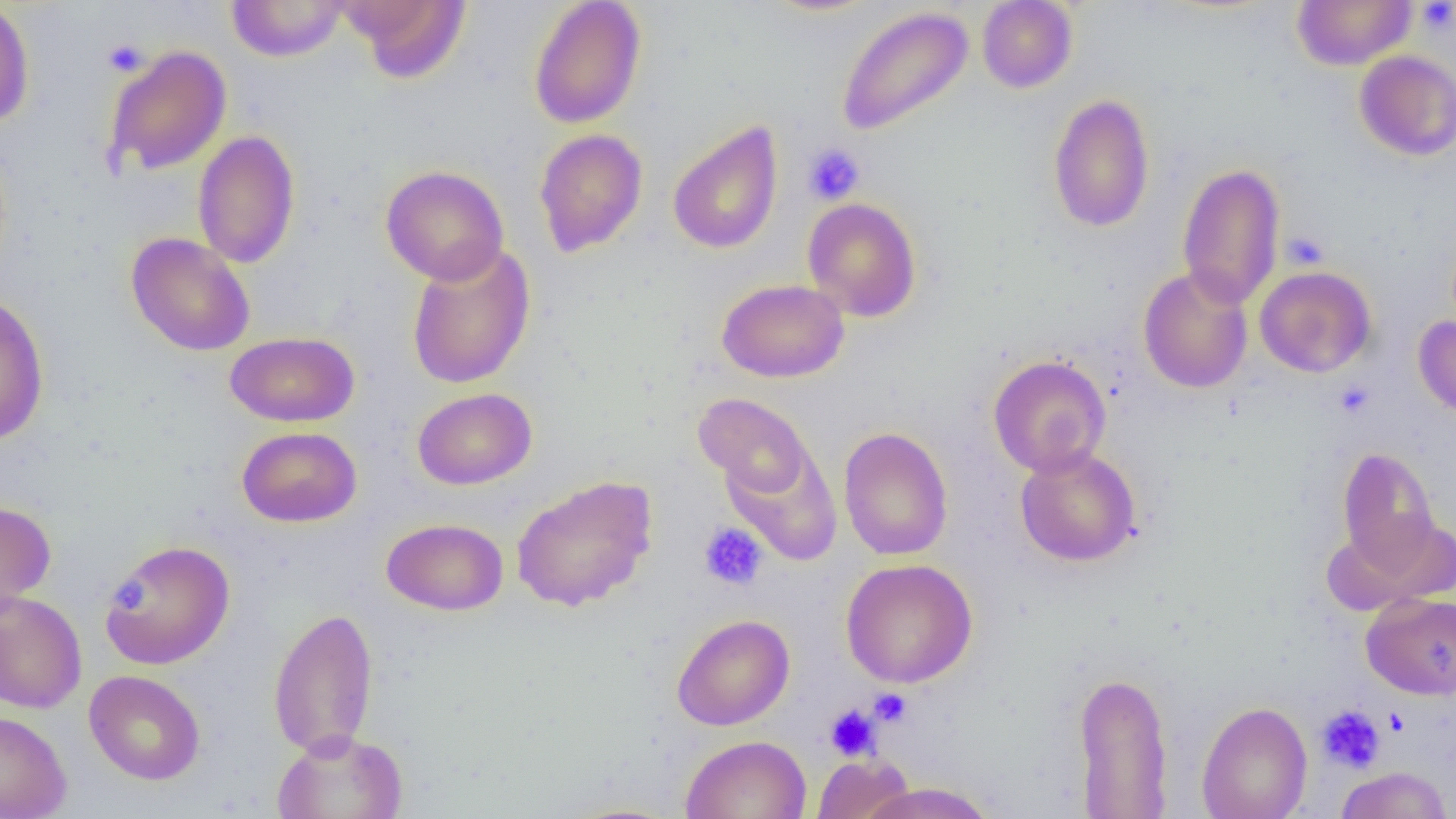

Summary:
  - Coordinate format: approximate bounding boxes as [x1, y1, x2, y2] in pixels
  - Platelet locations: [1416, 1, 1456, 34], [103, 39, 148, 76], [802, 143, 866, 204], [1281, 231, 1329, 270], [1334, 381, 1374, 419], [699, 522, 768, 591], [108, 579, 146, 614], [869, 688, 911, 726], [824, 704, 881, 761], [1316, 704, 1386, 774], [1384, 708, 1410, 737]
  - Uninfected red blood cell locations: [0, 0, 35, 128], [338, 0, 472, 83], [529, 0, 647, 129], [760, 0, 883, 17], [977, 0, 1078, 92], [1291, 0, 1416, 70], [226, 1, 349, 62], [836, 5, 974, 137], [104, 45, 232, 176], [1354, 50, 1456, 160], [1047, 94, 1155, 233], [667, 121, 783, 255], [534, 128, 648, 258], [192, 130, 301, 269], [1176, 163, 1286, 308], [380, 165, 510, 286], [803, 197, 922, 322], [126, 232, 255, 356], [406, 240, 536, 390], [1138, 266, 1253, 393], [1254, 266, 1376, 377], [717, 278, 849, 383], [0, 292, 49, 445], [1413, 316, 1456, 418], [224, 331, 359, 427], [988, 355, 1111, 477], [412, 387, 537, 490], [693, 392, 815, 500], [237, 426, 362, 527], [838, 426, 953, 561], [721, 445, 842, 566], [1015, 446, 1142, 567], [1337, 448, 1440, 572], [511, 475, 658, 612], [0, 500, 56, 616], [1329, 515, 1454, 614], [381, 517, 508, 615], [100, 540, 234, 670], [840, 558, 978, 688], [0, 588, 87, 714], [1361, 593, 1456, 700], [268, 606, 379, 759], [671, 613, 795, 731], [84, 670, 206, 785], [1073, 670, 1173, 817], [1197, 701, 1312, 819], [1317, 706, 1386, 776], [0, 710, 72, 819], [271, 729, 409, 819], [680, 735, 812, 819], [812, 753, 914, 818], [1334, 766, 1453, 819], [856, 781, 997, 819]
  - Slide-level diagnosis: no evidence of blood parasites
  - Magnification: 1000x
  - Image size: 1456×819 pixels
  - Modality: light microscopy
  - Field of view: single
  - Preparation: thin blood film